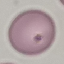
result = no malaria parasites seen
stain = Giemsa
capture = smartphone through the microscope eyepiece
image type = automatically extracted cell patch, resized to 64 × 64 pixels
preparation = thin smear